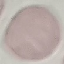
Malaria status: uninfected. Photographed with a smartphone camera at the microscope eyepiece. Giemsa-stained preparation. Cell patch, automatically extracted from a larger field of view and resized to 64 × 64 pixels. Thin blood film.